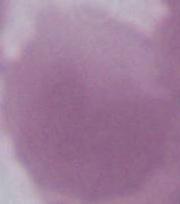
1000x magnification. An erythrocyte is shown. Micrograph.